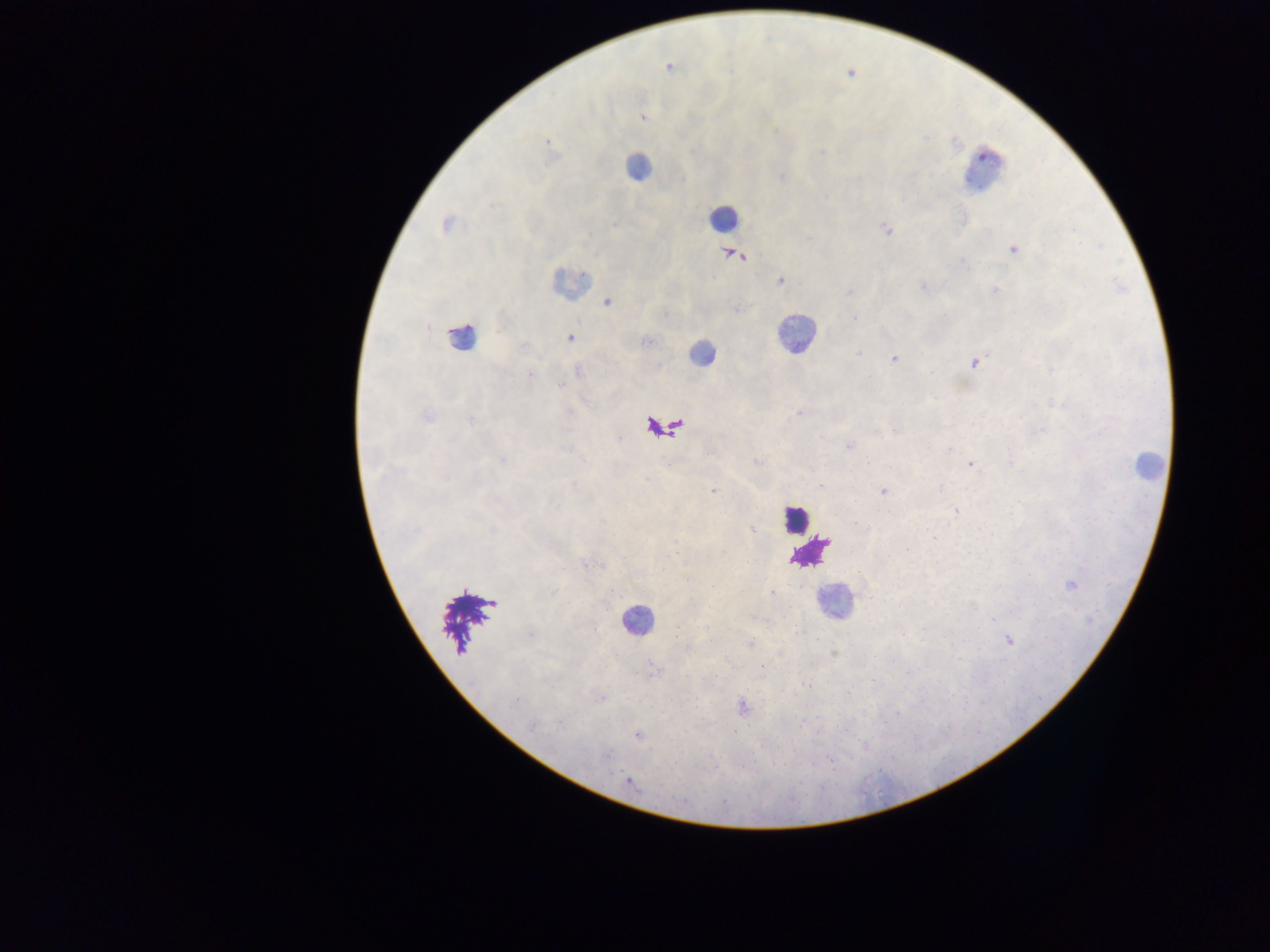 Approximate centers as (x, y) in pixels. Plasmodium parasite locations: (668, 67), (643, 117), (548, 141), (446, 224), (1074, 229), (887, 230), (1013, 249), (736, 255), (963, 263), (781, 281), (922, 286), (996, 290), (850, 292), (607, 302), (736, 309), (854, 318), (569, 338), (647, 341), (858, 353), (893, 358), (974, 362), (530, 374), (799, 413), (426, 416), (470, 420), (896, 431), (1041, 431), (848, 446), (568, 449), (949, 449), (503, 459), (756, 461), (971, 464), (820, 486), (941, 489), (713, 492), (884, 492), (955, 511), (856, 524), (752, 530), (492, 531), (935, 538), (907, 549), (670, 555), (1071, 585), (552, 591), (771, 592), (992, 619), (531, 635), (1009, 641), (750, 644), (762, 667), (808, 685), (601, 698), (515, 703), (742, 707), (802, 722), (560, 724), (532, 727), (637, 736), (628, 782). Leukocyte locations: (637, 167), (985, 169), (724, 218), (569, 282), (795, 334), (460, 337), (701, 353), (1147, 465), (794, 519), (832, 601), (636, 620). Photographed through a microscope with a mobile-phone camera. One field of view. Thick blood smear. Collected in Ghana. Image is 1270×952 pixels.